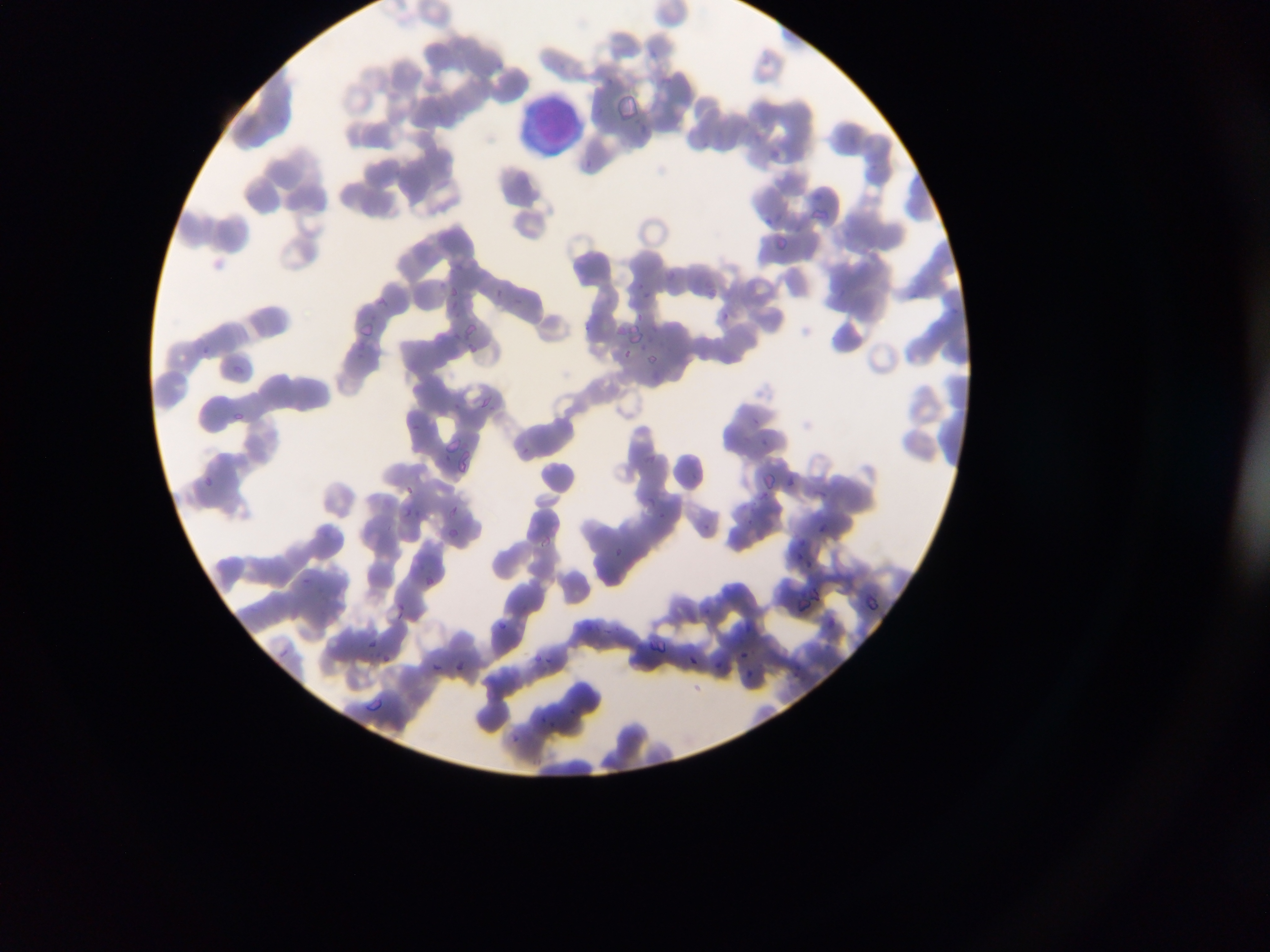

country = Ghana
leukocyte locations = approximate bounding boxes as (left, top, right, bottom) in pixels: (525, 100, 577, 152)
image size = 1270×952 pixels
field of view = single
malaria parasite locations = approximate bounding boxes as (left, top, right, bottom) in pixels: (614, 95, 641, 120), (578, 156, 598, 174), (811, 202, 837, 226), (772, 236, 789, 252), (634, 281, 645, 291), (445, 284, 463, 301), (642, 291, 656, 301), (445, 295, 464, 315), (720, 311, 734, 326), (637, 312, 649, 326), (451, 322, 480, 347), (583, 323, 595, 331), (447, 326, 469, 347), (623, 328, 647, 349), (352, 338, 373, 358), (626, 348, 635, 362), (647, 353, 663, 362), (482, 395, 493, 412), (451, 403, 462, 409), (232, 413, 242, 423), (751, 414, 762, 425), (411, 421, 423, 429), (760, 436, 774, 451), (523, 446, 537, 456), (443, 453, 454, 461), (760, 471, 775, 488), (789, 473, 799, 490), (202, 474, 217, 487), (406, 483, 413, 494), (759, 492, 771, 501), (645, 495, 659, 508), (451, 506, 462, 515), (402, 507, 415, 518), (660, 511, 670, 525), (818, 518, 832, 536), (446, 526, 463, 538), (537, 533, 554, 550), (616, 545, 628, 560), (793, 552, 802, 561), (805, 558, 816, 574), (301, 574, 310, 586), (422, 574, 435, 587), (396, 601, 404, 607), (398, 608, 406, 621), (500, 621, 512, 632), (366, 638, 379, 645), (655, 639, 670, 655), (737, 647, 749, 661), (380, 651, 391, 662), (534, 652, 542, 660), (688, 653, 700, 670), (538, 654, 556, 667), (428, 659, 443, 673), (451, 660, 468, 675), (717, 660, 728, 672), (747, 670, 756, 682), (368, 697, 385, 712), (568, 706, 577, 715), (539, 714, 546, 722), (546, 721, 557, 729), (512, 733, 521, 744)
capture = mobile-phone photograph through a microscope
preparation = thin blood film